State which cell type is depicted.
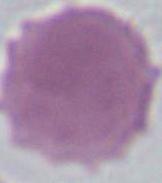
An erythrocyte.

1000x magnification. Photomicrograph.